Name the parasite shown.
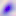
Toxoplasma gondii.

400x magnification. Photomicrograph.